State which parasite is depicted.
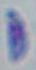
This is Toxoplasma gondii.

magnification = 1000x
modality = photomicrograph